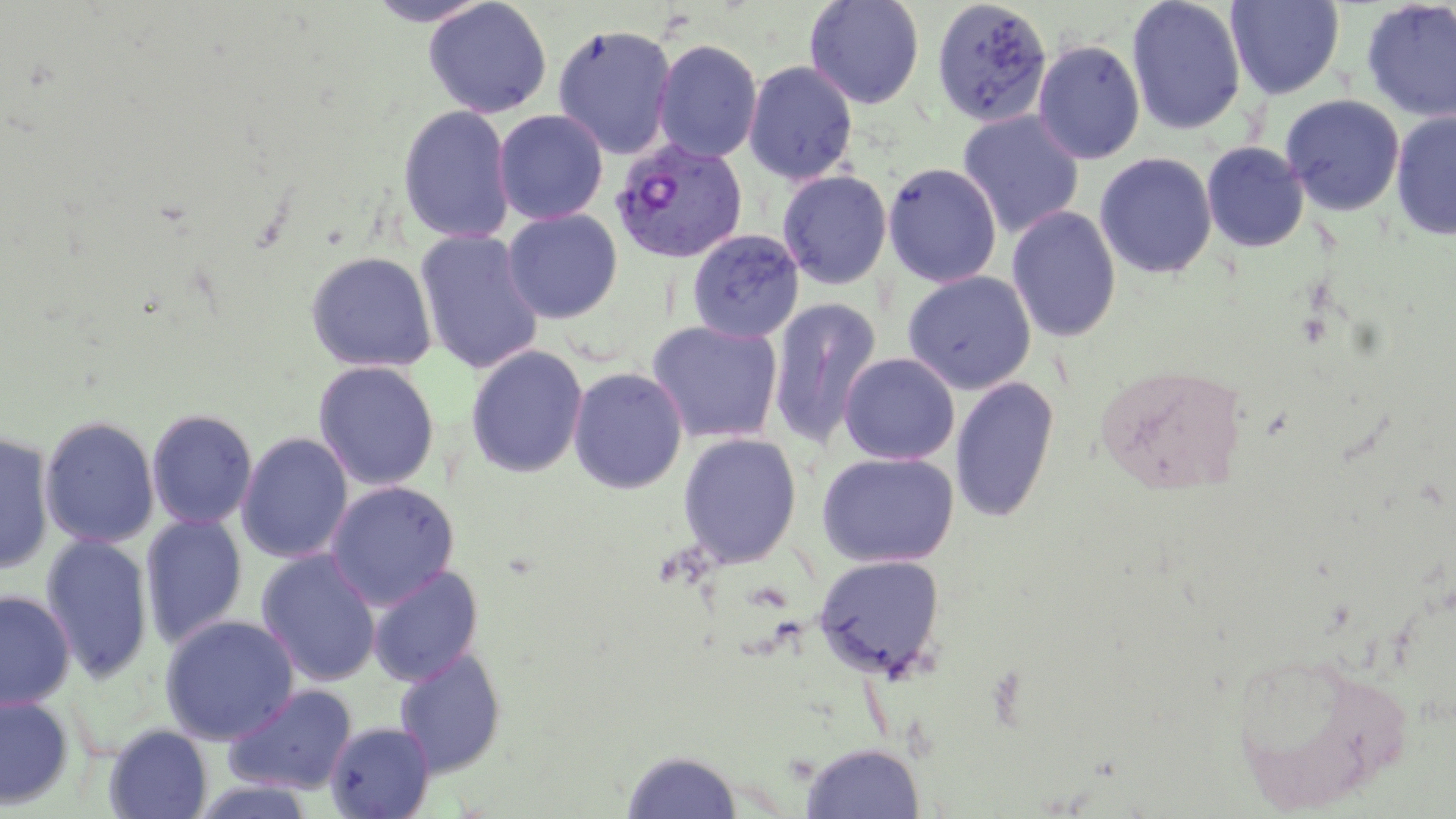

plasmodium_vivax_infected_red_blood_cell_locations: 'approximate bounding boxes as (x1, y1, x2, y2) in pixels: (610, 138, 747, 264)'
slide_level_diagnosis: Plasmodium vivax
stain: May-Grünwald-Giemsa
field_of_view: one of a larger specimen
image_size: 1456×819 pixels
magnification: 1000x
preparation: thin blood smear
uninfected_red_blood_cell_locations: 'approximate bounding boxes as (x1, y1, x2, y2) in pixels: (365, 0, 494, 27), (423, 0, 552, 118), (804, 0, 926, 110), (930, 0, 1052, 128), (1126, 0, 1248, 136), (1225, 0, 1345, 100), (1360, 0, 1456, 122), (553, 24, 677, 160), (653, 39, 762, 163), (1032, 39, 1146, 165), (743, 60, 859, 185), (1280, 94, 1405, 216), (398, 105, 515, 244), (493, 109, 609, 225), (957, 110, 1084, 239), (1390, 110, 1456, 241), (1201, 141, 1310, 252), (1094, 152, 1217, 279), (883, 162, 1002, 288), (777, 170, 893, 290), (1006, 205, 1122, 343), (502, 208, 623, 323), (686, 229, 805, 343), (414, 230, 544, 375), (305, 250, 437, 373), (902, 271, 1036, 394), (767, 299, 882, 448), (646, 319, 783, 445), (465, 344, 588, 478), (839, 352, 959, 465), (313, 360, 440, 491), (568, 366, 688, 494), (949, 375, 1060, 523), (146, 407, 258, 530), (39, 414, 160, 549), (0, 429, 55, 575), (236, 432, 354, 564), (678, 432, 802, 568), (816, 451, 959, 567), (325, 480, 460, 610), (140, 513, 249, 650), (40, 534, 155, 684), (256, 549, 381, 686), (813, 553, 946, 679), (367, 564, 484, 687), (0, 590, 76, 710), (160, 614, 300, 745), (1226, 647, 1416, 814), (393, 648, 507, 777), (223, 683, 358, 794), (0, 694, 75, 810), (326, 721, 435, 818), (103, 724, 213, 819), (801, 743, 924, 818), (620, 749, 743, 818)'
modality: light microscopy